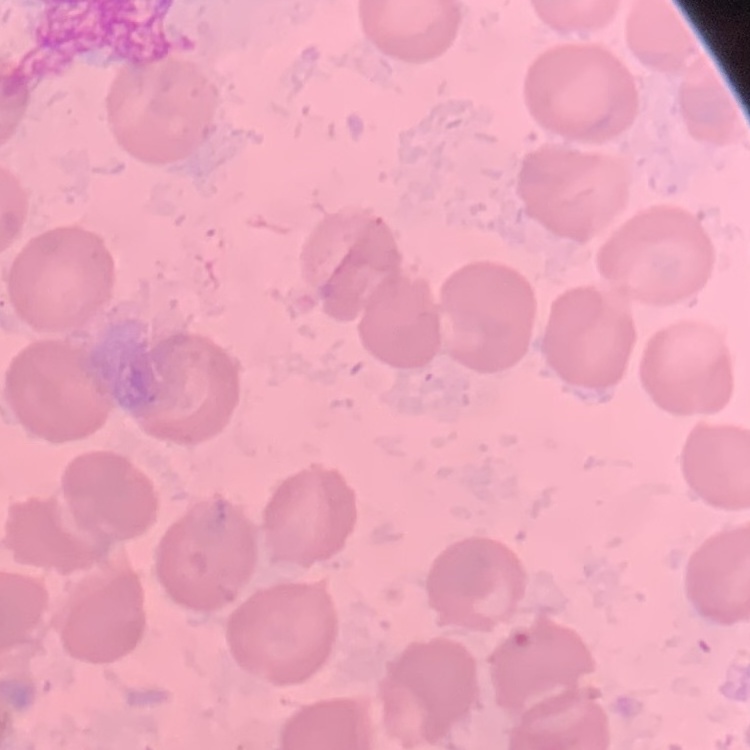
red blood cell morphology = no rouleaux formation
preparation = thin blood smear
image type = square crop of a larger photomicrograph
stain = Field's or Giemsa